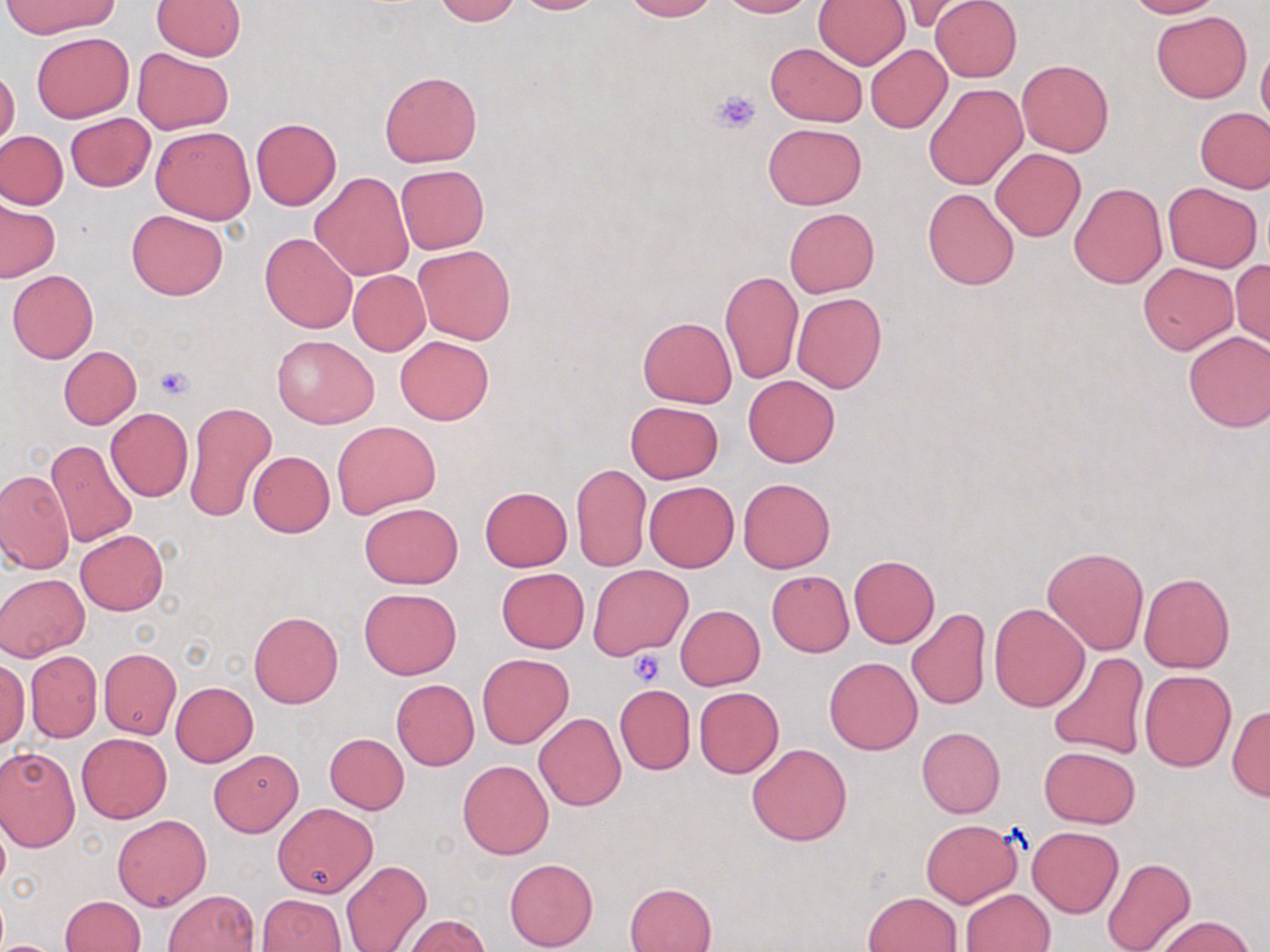
Summary:
  - Coordinate format: approximate bounding boxes as (x1, y1, x2, y2) in pixels
  - Uninfected red blood cell locations: (435, 0, 520, 25), (510, 0, 608, 14), (623, 0, 716, 21), (718, 0, 813, 17), (896, 0, 980, 33), (929, 0, 1020, 81), (1123, 0, 1221, 18), (2, 1, 120, 37), (153, 1, 245, 59), (815, 1, 910, 70), (1151, 11, 1251, 103), (31, 31, 134, 122), (1256, 40, 1270, 129), (767, 42, 868, 126), (866, 45, 952, 133), (131, 47, 234, 135), (1017, 59, 1113, 157), (0, 67, 20, 150), (380, 71, 482, 167), (925, 84, 1027, 190), (1195, 106, 1270, 193), (64, 113, 155, 193), (250, 118, 342, 209), (763, 122, 867, 209), (151, 126, 256, 224), (0, 130, 67, 209), (990, 148, 1086, 241), (395, 165, 489, 254), (311, 172, 413, 281), (1162, 181, 1263, 272), (1069, 183, 1167, 287), (923, 187, 1019, 290), (0, 201, 60, 282), (784, 207, 879, 297), (126, 210, 227, 299), (260, 232, 357, 333), (414, 244, 515, 345), (1230, 259, 1270, 347), (1138, 261, 1238, 354), (7, 270, 98, 364), (720, 270, 803, 383), (348, 271, 429, 355), (792, 293, 886, 394), (638, 316, 737, 407), (1182, 330, 1270, 432), (271, 334, 379, 428), (395, 335, 494, 424), (58, 346, 141, 429), (743, 374, 840, 468), (183, 401, 278, 525), (626, 401, 722, 483), (105, 407, 192, 502), (332, 420, 440, 517), (45, 439, 139, 548), (248, 451, 334, 537), (572, 463, 651, 572), (0, 468, 75, 573), (739, 477, 836, 573), (644, 481, 740, 572), (479, 486, 573, 572), (359, 501, 463, 589), (75, 530, 169, 615), (1042, 547, 1149, 654), (849, 556, 939, 647), (587, 564, 693, 659), (496, 568, 588, 652), (766, 570, 854, 657), (1138, 572, 1234, 672), (0, 573, 89, 661), (358, 587, 462, 678), (988, 603, 1089, 712), (675, 605, 764, 690), (906, 609, 991, 711), (250, 611, 342, 708), (99, 648, 181, 739), (27, 651, 102, 741), (1048, 652, 1151, 759), (478, 653, 573, 747), (824, 656, 923, 754), (0, 657, 29, 749), (1139, 670, 1235, 771), (391, 679, 479, 770), (170, 682, 258, 767), (615, 685, 695, 774), (694, 687, 784, 779), (1227, 705, 1270, 800), (534, 713, 626, 811), (917, 726, 1005, 817), (76, 733, 171, 822), (325, 733, 410, 814), (746, 742, 852, 845), (1039, 745, 1140, 828), (0, 747, 81, 850), (209, 750, 303, 836), (458, 760, 553, 859), (272, 802, 378, 898), (113, 814, 211, 911), (0, 817, 9, 894), (921, 818, 1022, 907), (1027, 826, 1123, 916), (504, 857, 598, 950), (1101, 858, 1196, 952), (341, 859, 431, 952), (625, 882, 716, 952), (961, 889, 1055, 952), (165, 890, 259, 952), (864, 891, 962, 952), (259, 893, 344, 952), (60, 895, 145, 951), (1152, 914, 1257, 952), (403, 915, 489, 952), (0, 940, 59, 951)
  - Platelet locations: (713, 88, 761, 132), (155, 364, 195, 400), (628, 650, 667, 686)
  - Slide-level diagnosis: negative for blood parasites
  - Field of view: one of a larger specimen
  - Preparation: thin blood smear
  - Image size: 1270×952 pixels
  - Magnification: 1000x
  - Stain: May-Grünwald-Giemsa
  - Modality: light microscopy